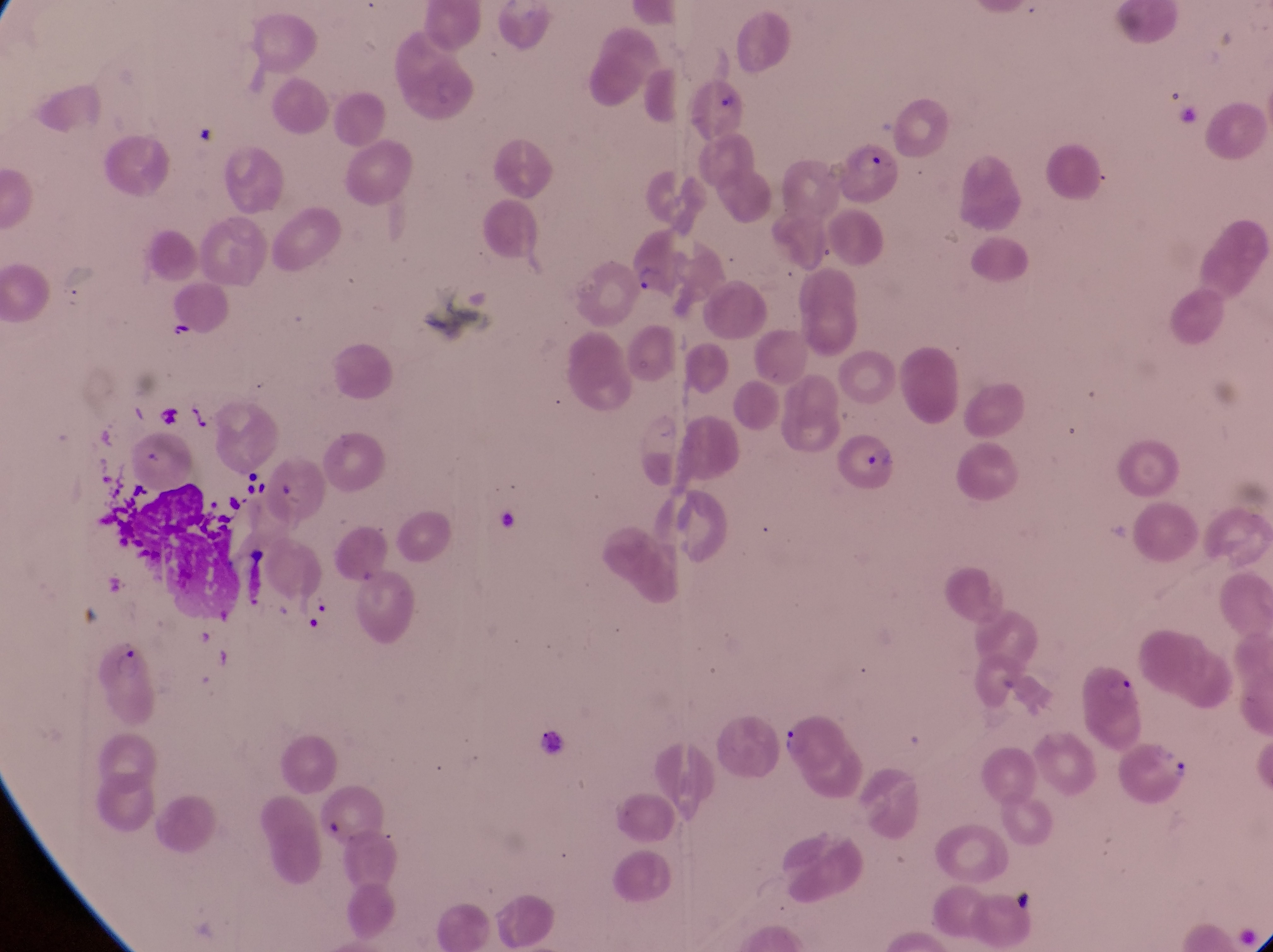

image size = 1273×952 pixels
magnification = 1000x
capture = smartphone photograph through the eyepiece of an Olympus CX-23 microscope
country = Uganda
preparation = thin blood film
parasitised red blood cell locations = approximate bounding boxes as {left, top, right, bottom} in pixels: {844, 145, 914, 213}, {631, 235, 694, 302}, {839, 434, 902, 501}, {1083, 662, 1146, 752}, {771, 711, 841, 779}, {1113, 737, 1195, 805}
field of view = single